Classify this cell by malaria status.
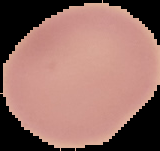

It is uninfected.

Summary:
  - Image type: segmented cell region on a black background
  - Preparation: thin blood smear
  - Image size: 160×151 pixels